Point out each malaria parasite and each leukocyte.
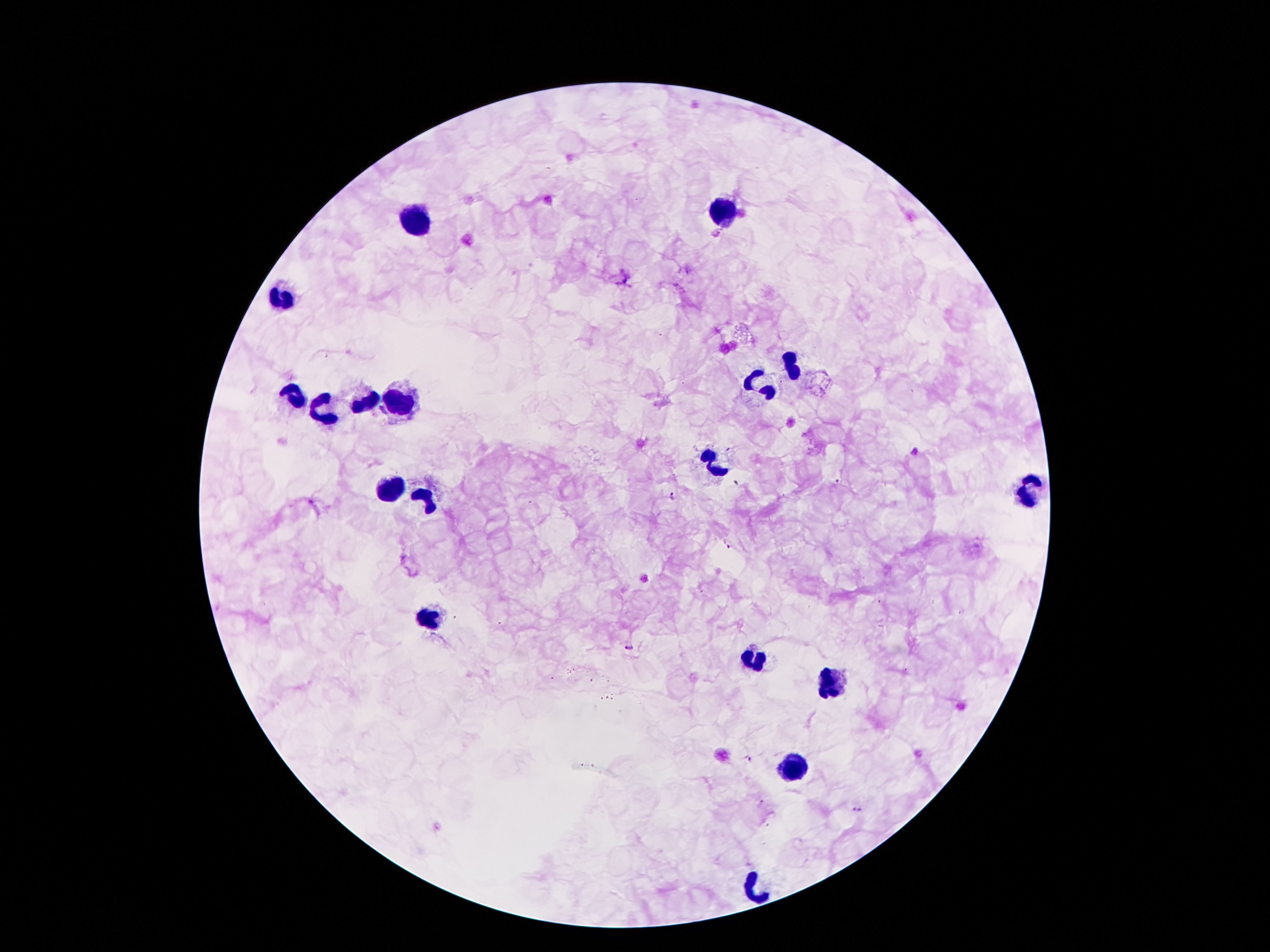
Approximate centers as {x, y} in pixels.
Malaria parasites: {915, 451}, {837, 483}, {671, 496}, {731, 546}, {631, 645}, {748, 757}, {759, 803}, {857, 810}.
Leukocytes: {726, 214}, {421, 220}, {285, 293}, {789, 363}, {764, 388}, {289, 394}, {365, 401}, {398, 403}, {321, 413}, {715, 464}, {394, 487}, {1032, 491}, {426, 495}, {430, 617}, {753, 659}, {837, 682}, {797, 764}, {757, 888}.

field of view = one from this slide
capture = smartphone camera through the microscope eyepiece
magnification = 100x
image size = 1270×952 pixels
patient malaria status = infected with Plasmodium falciparum
stain = Giemsa
preparation = thick blood film